Outline each blood parasite and name the species.
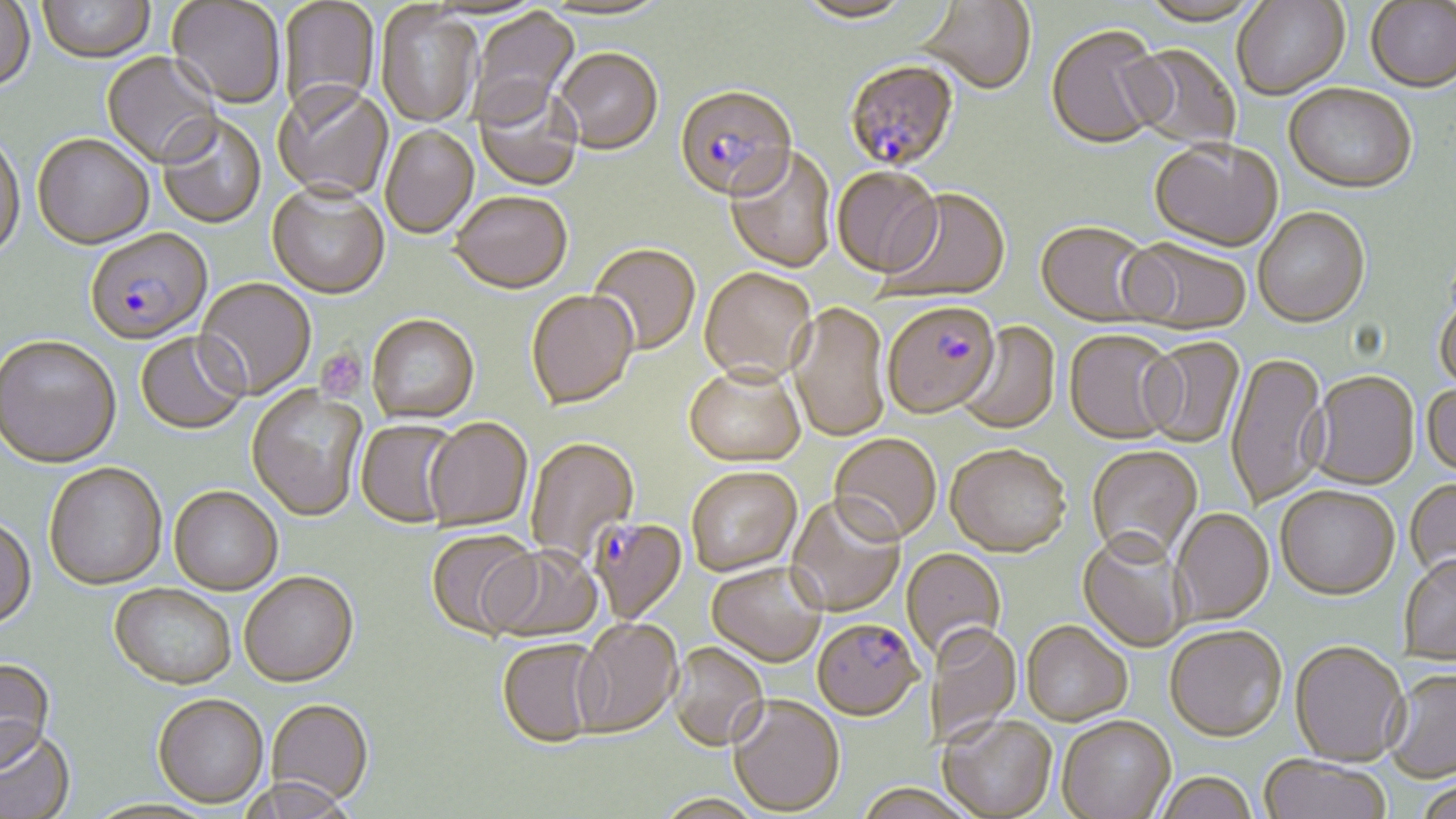
Approximate bounding boxes as (x1, y1, x2, y2) in pixels.
Plasmodium falciparum-infected red blood cells: (844, 62, 960, 175), (674, 88, 797, 206), (85, 231, 212, 347), (882, 304, 1001, 421), (590, 518, 687, 625), (811, 621, 923, 724).
No Plasmodium ovale, Plasmodium malariae, Plasmodium vivax, Babesia divergens, or Trypanosoma brucei observed.

Platelet locations: (316, 347, 366, 400). Uninfected red blood cell locations: (795, 0, 915, 26), (1232, 0, 1350, 101), (0, 1, 35, 94), (38, 1, 156, 65), (167, 1, 285, 110), (278, 1, 380, 122), (541, 1, 671, 23), (919, 1, 1037, 97), (1139, 1, 1262, 28), (1365, 2, 1456, 94), (375, 5, 482, 129), (468, 8, 581, 129), (1046, 27, 1167, 152), (1125, 44, 1242, 151), (554, 51, 663, 158), (101, 53, 223, 170), (272, 86, 394, 202), (473, 87, 583, 192), (1283, 87, 1417, 197), (157, 115, 267, 230), (380, 127, 479, 239), (0, 134, 26, 266), (33, 137, 154, 252), (1149, 141, 1283, 255), (724, 148, 837, 275), (832, 169, 943, 280), (267, 186, 389, 301), (879, 190, 1011, 306), (449, 194, 572, 297), (1253, 209, 1371, 331), (1034, 224, 1159, 330), (1121, 240, 1251, 337), (588, 245, 701, 358), (699, 270, 817, 390), (195, 280, 316, 400), (1434, 290, 1456, 397), (526, 292, 638, 412), (788, 304, 890, 444), (366, 316, 480, 426), (956, 322, 1061, 437), (1064, 332, 1182, 447), (136, 333, 249, 437), (0, 338, 121, 471), (1140, 339, 1245, 449), (1226, 353, 1329, 511), (683, 368, 806, 471), (1308, 373, 1420, 492), (1422, 384, 1456, 481), (246, 386, 367, 523), (355, 420, 460, 529), (424, 420, 533, 531), (828, 436, 941, 549), (525, 439, 639, 561), (945, 448, 1071, 561), (1086, 448, 1203, 568), (44, 465, 167, 592), (686, 469, 802, 579), (1405, 479, 1456, 587), (169, 489, 282, 597), (1276, 489, 1400, 603), (785, 497, 906, 620), (1171, 510, 1275, 627), (0, 519, 37, 631), (425, 531, 539, 641), (1077, 534, 1190, 654), (484, 547, 604, 644), (902, 549, 1007, 665), (1398, 556, 1456, 668), (706, 565, 826, 669), (240, 575, 359, 691), (110, 586, 235, 692), (571, 620, 683, 739), (1021, 624, 1132, 728), (930, 625, 1021, 745), (1165, 629, 1287, 746), (495, 639, 604, 749), (669, 644, 769, 754), (1289, 644, 1409, 769), (0, 660, 56, 775), (1384, 670, 1456, 783), (152, 697, 268, 810), (727, 698, 845, 817), (266, 701, 374, 807), (938, 718, 1058, 819), (1057, 718, 1176, 819), (0, 731, 75, 819), (1259, 757, 1391, 819), (1154, 775, 1259, 819), (239, 779, 357, 819), (1415, 782, 1456, 819). Slide-level diagnosis: Plasmodium falciparum. Captured at 1000x magnification. Image is 1456×819 pixels. May-Grünwald-Giemsa-stained preparation. Thin blood smear. Optical microscopy. One field of a larger specimen.